Locate every leukocyte (white blood cell).
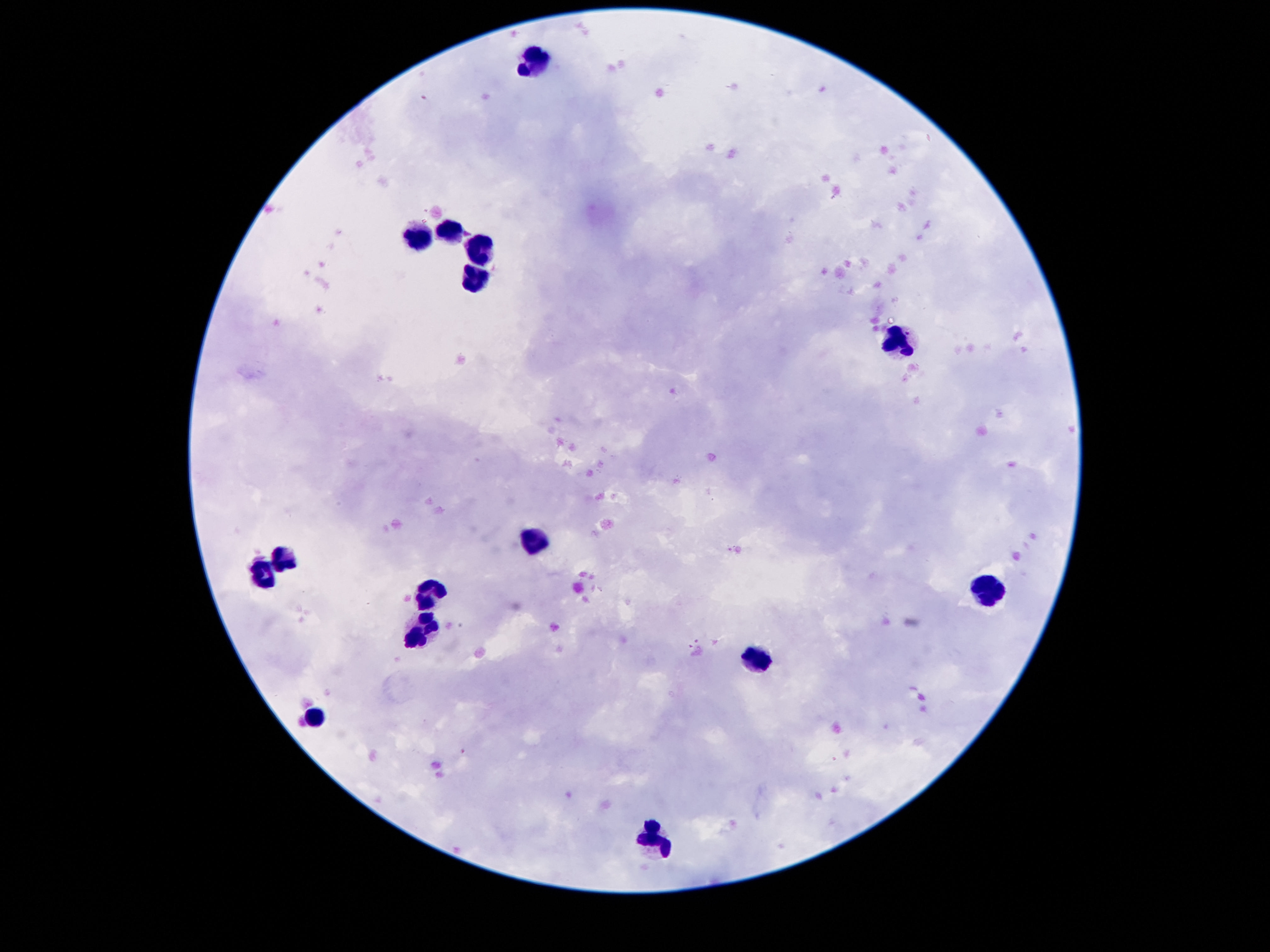
Approximate centers as [x, y] in pixels.
Leukocytes: [534, 62], [450, 230], [416, 238], [480, 247], [478, 274], [900, 342], [536, 539], [280, 557], [268, 573], [988, 591], [432, 593], [418, 633], [756, 659], [318, 719], [652, 837].

Summary:
  - Magnification: 100x
  - Field of view: one from this slide
  - Stain: Giemsa
  - Capture: smartphone camera through the microscope eyepiece
  - Patient malaria status: uninfected
  - Preparation: thick peripheral-blood smear
  - Image size: 1270×952 pixels